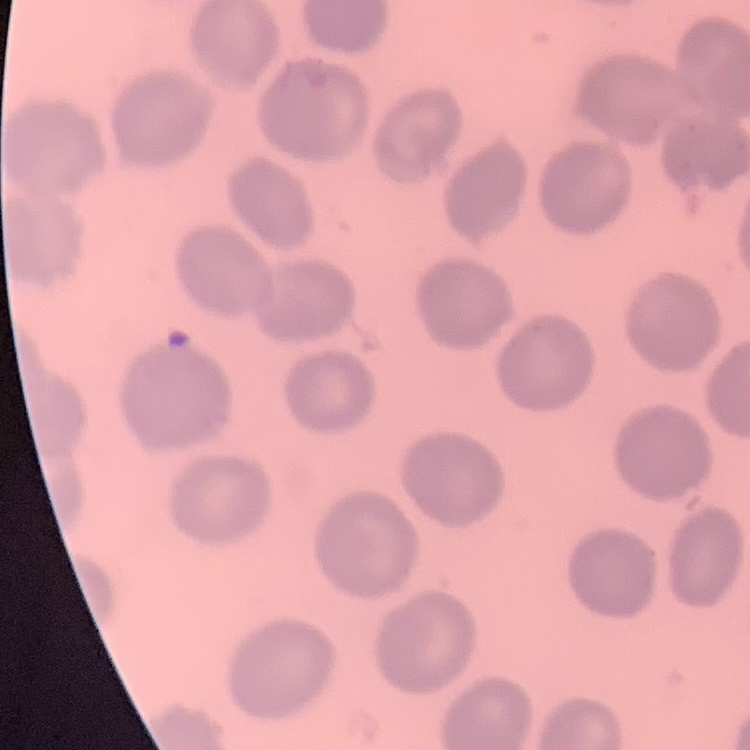
{
  "red_blood_cell_morphology": "no rouleaux formation",
  "image_type": "one tile cut from a larger photomicrograph",
  "stain": "Field's or Giemsa",
  "preparation": "thin peripheral smear"
}